Locate every uninfected red blood cell.
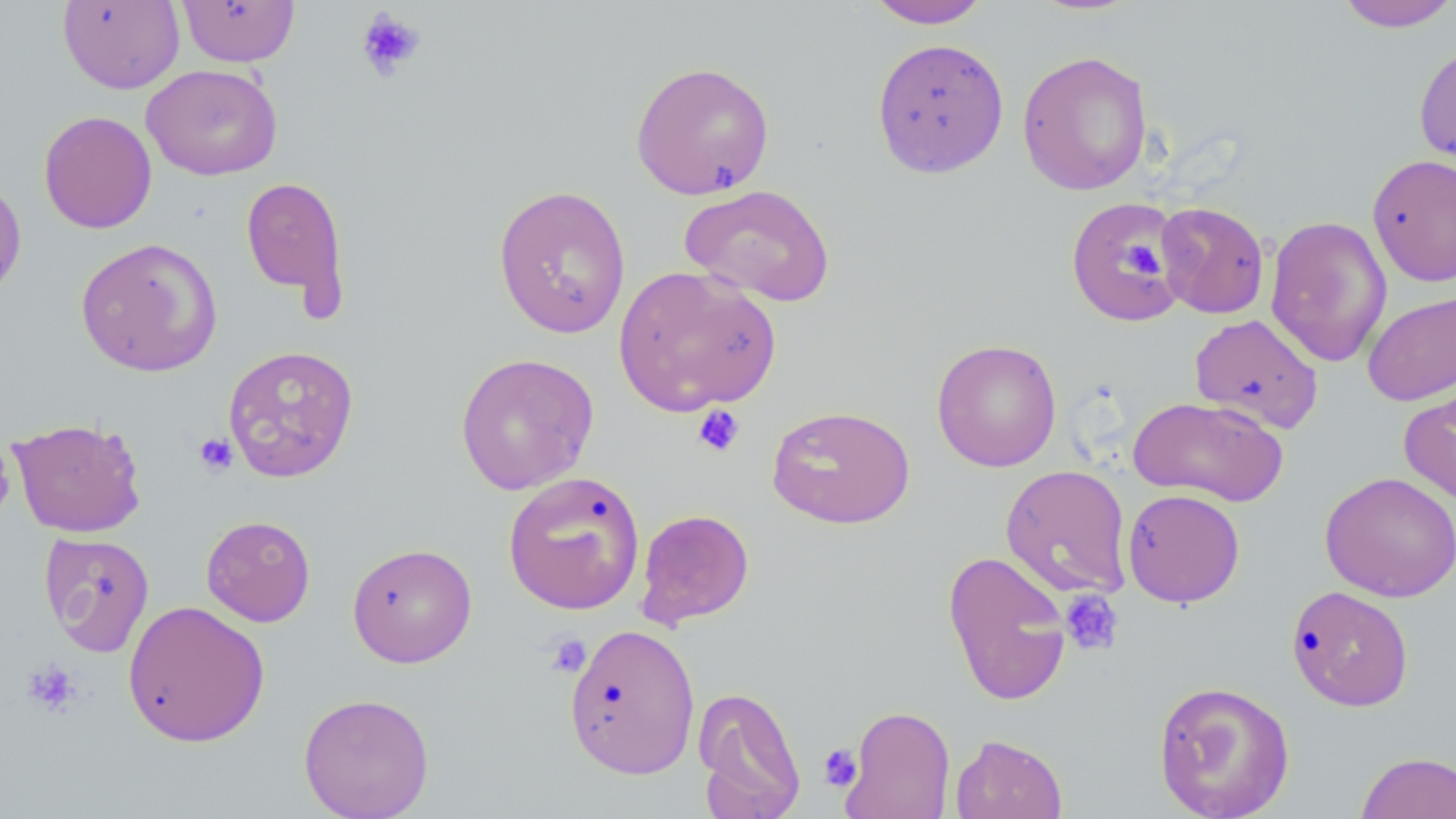

Approximate bounding boxes as named x1/y1/x2/y2 corners in pixels.
Uninfected red blood cells: (x1=177, y1=0, x2=300, y2=67), (x1=865, y1=0, x2=992, y2=28), (x1=57, y1=1, x2=185, y2=94), (x1=1334, y1=1, x2=1456, y2=33), (x1=871, y1=37, x2=1009, y2=178), (x1=1414, y1=41, x2=1456, y2=180), (x1=1016, y1=49, x2=1153, y2=196), (x1=629, y1=61, x2=776, y2=200), (x1=141, y1=63, x2=284, y2=181), (x1=38, y1=110, x2=157, y2=234), (x1=1367, y1=153, x2=1456, y2=287), (x1=0, y1=172, x2=27, y2=306), (x1=240, y1=175, x2=351, y2=315), (x1=493, y1=183, x2=632, y2=338), (x1=679, y1=183, x2=836, y2=307), (x1=1064, y1=196, x2=1184, y2=327), (x1=1155, y1=201, x2=1269, y2=319), (x1=1265, y1=215, x2=1392, y2=367), (x1=75, y1=236, x2=223, y2=378), (x1=613, y1=264, x2=781, y2=417), (x1=1362, y1=289, x2=1456, y2=407), (x1=1189, y1=313, x2=1324, y2=434), (x1=932, y1=338, x2=1062, y2=472), (x1=222, y1=344, x2=360, y2=483), (x1=454, y1=351, x2=599, y2=496), (x1=1399, y1=372, x2=1456, y2=506), (x1=1128, y1=395, x2=1288, y2=506), (x1=766, y1=405, x2=915, y2=529), (x1=8, y1=417, x2=147, y2=538), (x1=1000, y1=464, x2=1133, y2=599), (x1=503, y1=471, x2=645, y2=615), (x1=1319, y1=471, x2=1456, y2=602), (x1=1122, y1=488, x2=1246, y2=608), (x1=635, y1=508, x2=755, y2=629), (x1=201, y1=515, x2=316, y2=626), (x1=39, y1=532, x2=155, y2=657), (x1=347, y1=542, x2=477, y2=668), (x1=941, y1=550, x2=1074, y2=707), (x1=1286, y1=585, x2=1414, y2=711), (x1=122, y1=600, x2=271, y2=748), (x1=563, y1=623, x2=701, y2=779), (x1=1152, y1=679, x2=1295, y2=819), (x1=692, y1=685, x2=806, y2=819), (x1=297, y1=692, x2=435, y2=818), (x1=841, y1=704, x2=956, y2=819), (x1=950, y1=733, x2=1068, y2=819), (x1=1355, y1=751, x2=1456, y2=819).

Platelet locations: (x1=356, y1=7, x2=427, y2=82), (x1=1124, y1=242, x2=1163, y2=279), (x1=692, y1=404, x2=746, y2=458), (x1=193, y1=432, x2=238, y2=476), (x1=1060, y1=590, x2=1124, y2=656), (x1=545, y1=632, x2=591, y2=678), (x1=22, y1=660, x2=80, y2=717), (x1=818, y1=743, x2=863, y2=790). Slide-level diagnosis: no evidence of blood parasites. Captured at 1000x magnification. Light microscopy. Thin blood smear. Image is 1456×819 pixels. May-Grünwald-Giemsa-stained preparation. Single field of view.